Report the malaria status of this cell.
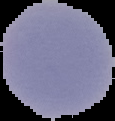
It is uninfected.

{
  "image_size": "115×121 pixels",
  "preparation": "thin blood smear",
  "image_type": "cell region segmented out of the field of view; surrounding area masked to black"
}